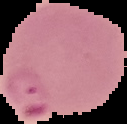

From a thin blood film. Result: malaria parasites detected. Cell region segmented out of the field of view; the surrounding area is masked to black. Image is 127×124 pixels.